Locate and identify every blood parasite.
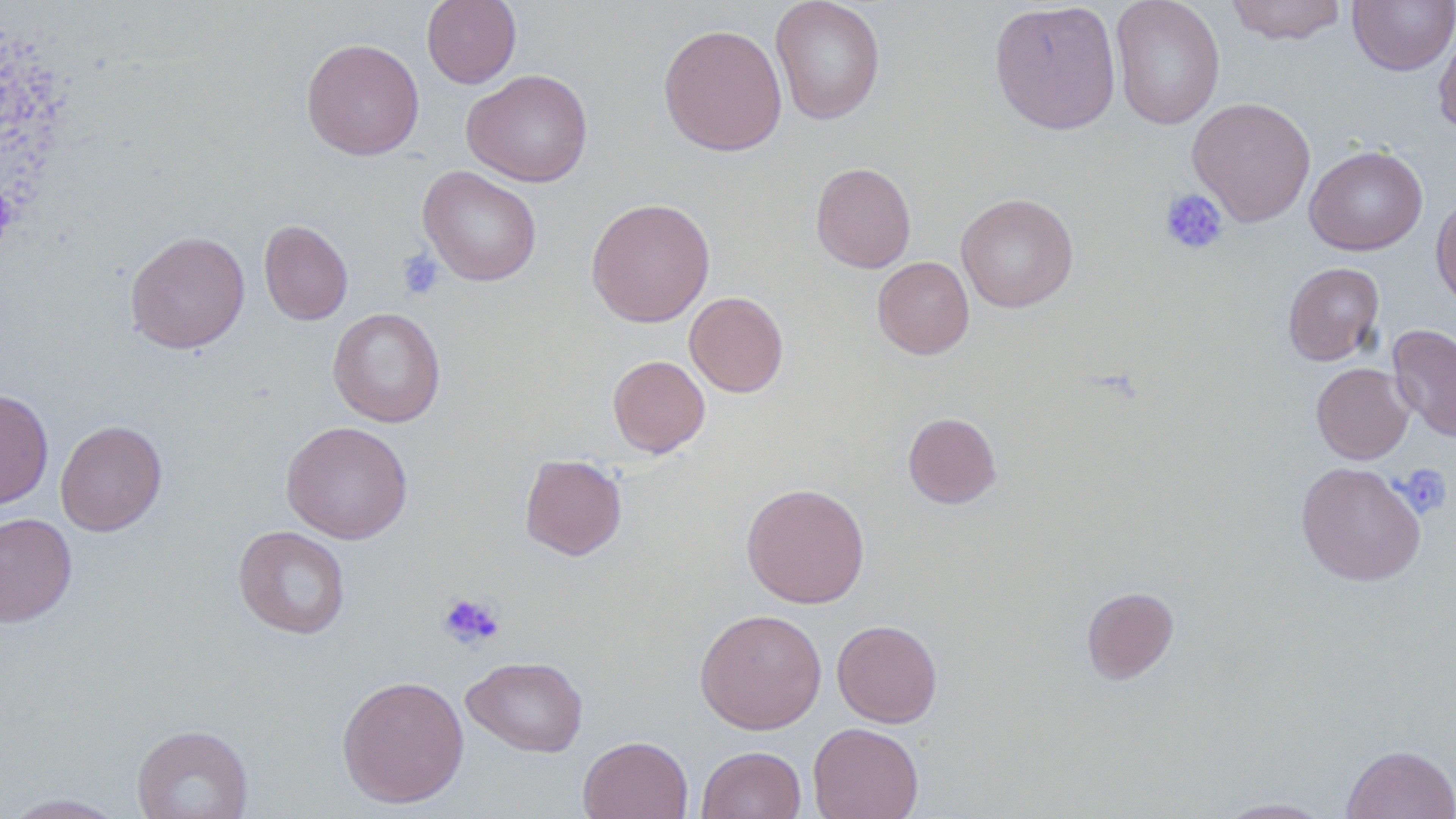

No blood parasites observed.

{
  "slide_level_diagnosis": "no evidence of blood parasites",
  "platelet_locations": "approximate bounding boxes as named x1/y1/x2/y2 corners in pixels: (x1=1159, y1=188, x2=1228, y2=255), (x1=397, y1=250, x2=444, y2=300), (x1=1396, y1=463, x2=1452, y2=518), (x1=437, y1=591, x2=505, y2=650)",
  "magnification": "1000x",
  "uninfected_red_blood_cell_locations": "approximate bounding boxes as named x1/y1/x2/y2 corners in pixels: (x1=422, y1=0, x2=522, y2=88), (x1=770, y1=0, x2=885, y2=125), (x1=1110, y1=0, x2=1225, y2=130), (x1=1225, y1=0, x2=1347, y2=45), (x1=1348, y1=0, x2=1456, y2=74), (x1=988, y1=1, x2=1122, y2=135), (x1=658, y1=23, x2=787, y2=156), (x1=1434, y1=27, x2=1456, y2=138), (x1=300, y1=38, x2=425, y2=160), (x1=462, y1=68, x2=593, y2=188), (x1=1187, y1=97, x2=1316, y2=225), (x1=1305, y1=145, x2=1427, y2=255), (x1=810, y1=162, x2=916, y2=273), (x1=418, y1=166, x2=542, y2=286), (x1=1431, y1=192, x2=1456, y2=308), (x1=956, y1=193, x2=1078, y2=312), (x1=585, y1=197, x2=715, y2=327), (x1=259, y1=220, x2=353, y2=325), (x1=124, y1=230, x2=250, y2=354), (x1=871, y1=256, x2=974, y2=359), (x1=1282, y1=262, x2=1385, y2=365), (x1=684, y1=291, x2=788, y2=397), (x1=328, y1=307, x2=446, y2=427), (x1=1388, y1=323, x2=1456, y2=443), (x1=608, y1=355, x2=710, y2=457), (x1=1311, y1=363, x2=1413, y2=464), (x1=0, y1=388, x2=53, y2=510), (x1=903, y1=412, x2=1002, y2=508), (x1=55, y1=419, x2=167, y2=536), (x1=281, y1=421, x2=413, y2=544), (x1=520, y1=454, x2=627, y2=560), (x1=1296, y1=461, x2=1426, y2=586), (x1=741, y1=482, x2=870, y2=608), (x1=0, y1=512, x2=77, y2=627), (x1=233, y1=525, x2=351, y2=639), (x1=1081, y1=587, x2=1179, y2=683), (x1=695, y1=609, x2=827, y2=734), (x1=832, y1=620, x2=943, y2=728), (x1=462, y1=655, x2=589, y2=757), (x1=337, y1=675, x2=469, y2=808), (x1=808, y1=722, x2=923, y2=819), (x1=131, y1=724, x2=253, y2=819), (x1=578, y1=735, x2=693, y2=819), (x1=696, y1=745, x2=806, y2=819), (x1=1341, y1=745, x2=1456, y2=818), (x1=1, y1=793, x2=131, y2=818), (x1=1217, y1=797, x2=1334, y2=818)",
  "modality": "light microscopy",
  "image_size": "1456×819 pixels",
  "stain": "May-Grünwald-Giemsa",
  "field_of_view": "one of a larger specimen",
  "preparation": "thin blood film"
}